Give the position of every Plasmodium parasite.
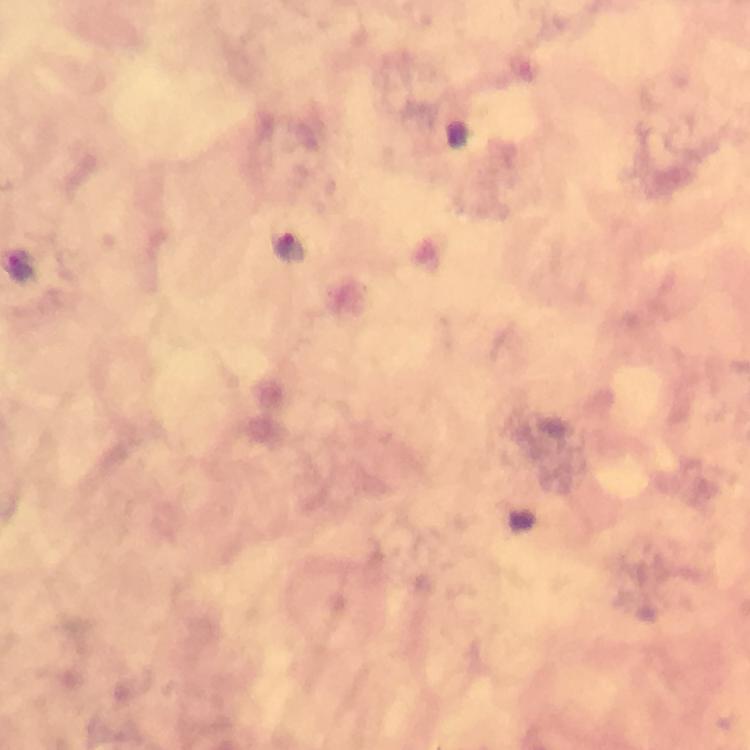

Approximate centers as (x, y) in pixels.
Plasmodium parasites: (288, 249).

Immersion oil was used. A crop from one field of view. Giemsa-stained preparation. At 100x magnification. Thick blood smear. Image is 750×750 pixels. From a diagnostic examination for malaria. Smartphone photograph taken through a microscope.